Give the extent of all Plasmodium vivax-infected red blood cells.
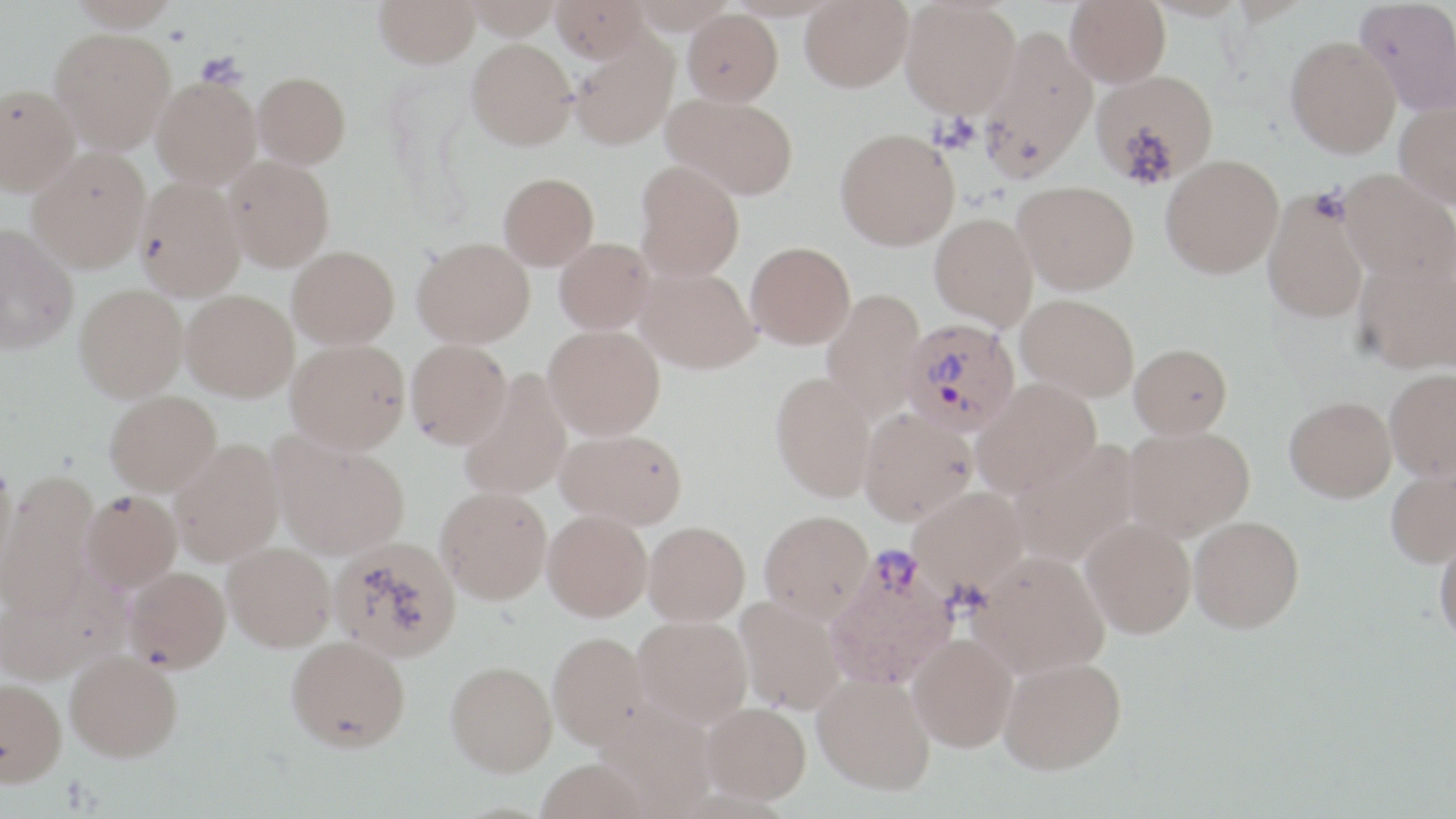

Approximate bounding boxes as named x1/y1/x2/y2 corners in pixels.
Plasmodium vivax-infected red blood cells: (x1=901, y1=317, x2=1021, y2=437), (x1=824, y1=546, x2=960, y2=689).

Summary:
  - Uninfected red blood cell locations: (x1=69, y1=0, x2=178, y2=31), (x1=463, y1=0, x2=562, y2=39), (x1=550, y1=0, x2=651, y2=63), (x1=631, y1=0, x2=736, y2=32), (x1=801, y1=0, x2=913, y2=92), (x1=1065, y1=0, x2=1170, y2=87), (x1=1144, y1=0, x2=1250, y2=21), (x1=1355, y1=0, x2=1456, y2=115), (x1=374, y1=1, x2=481, y2=68), (x1=901, y1=1, x2=1021, y2=117), (x1=682, y1=9, x2=783, y2=105), (x1=980, y1=26, x2=1097, y2=179), (x1=51, y1=29, x2=175, y2=153), (x1=1285, y1=35, x2=1400, y2=157), (x1=569, y1=36, x2=678, y2=151), (x1=467, y1=38, x2=577, y2=149), (x1=1092, y1=69, x2=1219, y2=186), (x1=253, y1=71, x2=351, y2=168), (x1=152, y1=76, x2=261, y2=188), (x1=0, y1=83, x2=79, y2=195), (x1=663, y1=94, x2=799, y2=199), (x1=1395, y1=101, x2=1456, y2=208), (x1=835, y1=128, x2=959, y2=250), (x1=28, y1=148, x2=150, y2=272), (x1=1161, y1=154, x2=1284, y2=277), (x1=224, y1=156, x2=335, y2=270), (x1=635, y1=160, x2=745, y2=280), (x1=1340, y1=169, x2=1456, y2=284), (x1=498, y1=172, x2=599, y2=269), (x1=136, y1=178, x2=246, y2=301), (x1=1014, y1=180, x2=1139, y2=294), (x1=1263, y1=192, x2=1368, y2=323), (x1=930, y1=213, x2=1038, y2=329), (x1=1, y1=224, x2=79, y2=353), (x1=412, y1=237, x2=535, y2=347), (x1=554, y1=238, x2=654, y2=333), (x1=746, y1=241, x2=856, y2=349), (x1=287, y1=246, x2=399, y2=349), (x1=1354, y1=258, x2=1456, y2=374), (x1=635, y1=266, x2=759, y2=373), (x1=75, y1=284, x2=188, y2=401), (x1=821, y1=289, x2=926, y2=420), (x1=181, y1=290, x2=298, y2=400), (x1=1016, y1=293, x2=1140, y2=401), (x1=544, y1=324, x2=665, y2=439), (x1=286, y1=339, x2=410, y2=452), (x1=406, y1=339, x2=512, y2=448), (x1=1129, y1=343, x2=1232, y2=438), (x1=459, y1=369, x2=572, y2=499), (x1=1384, y1=369, x2=1456, y2=480), (x1=771, y1=370, x2=878, y2=502), (x1=971, y1=379, x2=1102, y2=496), (x1=105, y1=390, x2=221, y2=496), (x1=1285, y1=395, x2=1396, y2=501), (x1=858, y1=408, x2=977, y2=525), (x1=1123, y1=425, x2=1254, y2=540), (x1=556, y1=427, x2=688, y2=529), (x1=270, y1=434, x2=409, y2=560), (x1=169, y1=439, x2=284, y2=565), (x1=1009, y1=440, x2=1139, y2=566), (x1=0, y1=457, x2=17, y2=578), (x1=1385, y1=461, x2=1456, y2=569), (x1=2, y1=469, x2=98, y2=615), (x1=436, y1=486, x2=552, y2=604), (x1=908, y1=486, x2=1029, y2=598), (x1=81, y1=490, x2=181, y2=590), (x1=543, y1=509, x2=652, y2=621), (x1=759, y1=509, x2=874, y2=621), (x1=1189, y1=515, x2=1304, y2=632), (x1=1082, y1=517, x2=1196, y2=638), (x1=643, y1=521, x2=750, y2=625), (x1=1434, y1=531, x2=1456, y2=645), (x1=328, y1=537, x2=461, y2=662), (x1=223, y1=542, x2=336, y2=651), (x1=969, y1=550, x2=1109, y2=678), (x1=124, y1=567, x2=230, y2=672), (x1=0, y1=576, x2=125, y2=685), (x1=736, y1=596, x2=846, y2=714), (x1=633, y1=615, x2=753, y2=726), (x1=548, y1=631, x2=652, y2=750), (x1=908, y1=633, x2=1017, y2=752), (x1=286, y1=635, x2=411, y2=752), (x1=64, y1=651, x2=183, y2=761), (x1=998, y1=656, x2=1126, y2=774), (x1=445, y1=660, x2=558, y2=776), (x1=813, y1=671, x2=936, y2=795), (x1=0, y1=678, x2=66, y2=786), (x1=595, y1=700, x2=716, y2=816), (x1=702, y1=702, x2=810, y2=804)
  - Platelet locations: (x1=197, y1=52, x2=245, y2=87)
  - Slide-level diagnosis: Plasmodium vivax
  - Image size: 1456×819 pixels
  - Field of view: one of a larger specimen
  - Preparation: thin blood film
  - Modality: light microscopy
  - Stain: May-Grünwald-Giemsa
  - Magnification: 1000x